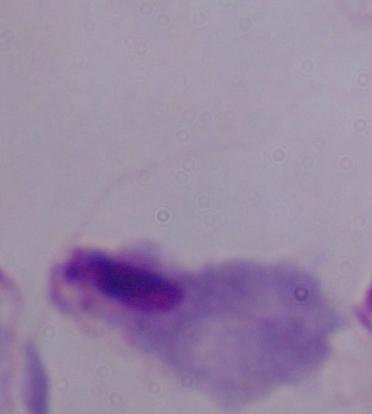

magnification = 1000x
identification = trichomonad
modality = photomicrograph